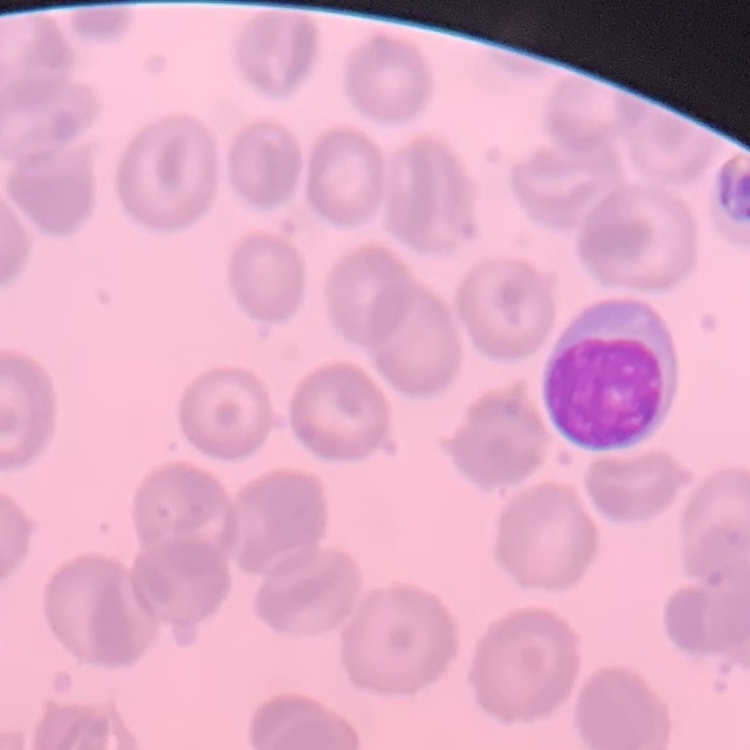

erythrocyte morphology = no rouleaux formation
preparation = thin blood smear
image type = square crop of a larger photomicrograph
stain = Field's or Giemsa